Report the malaria status of this cell.
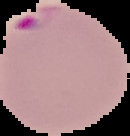
It is parasitized.

preparation = thin blood film
image size = 130×136 pixels
image type = cell region segmented out of the field of view; surrounding area masked to black